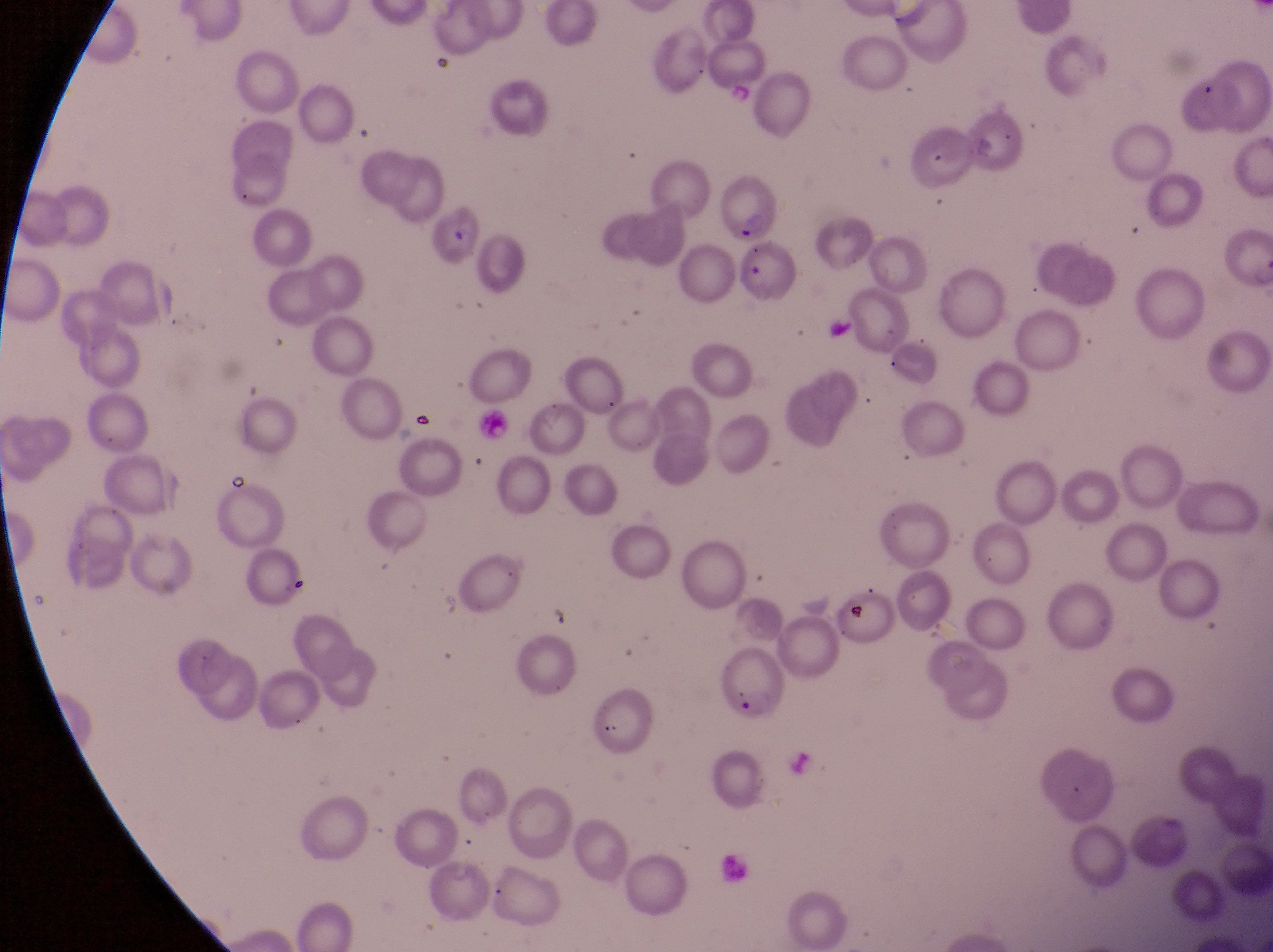

Approximate bounding boxes as (left, top, right, bottom) in pixels. Artifact (platelet-like body, stain precipitate, or debris) locations: (847, 600, 874, 628). Parasitised red blood cell locations: (714, 169, 777, 241), (429, 204, 481, 264), (736, 242, 798, 307), (717, 641, 790, 724). Thin blood smear. At a magnification of 1000x. Image is 1273×952 pixels. Single field of view. Captured by a smartphone held over the eyepiece of an Olympus CX-23 microscope. Sample from Uganda.